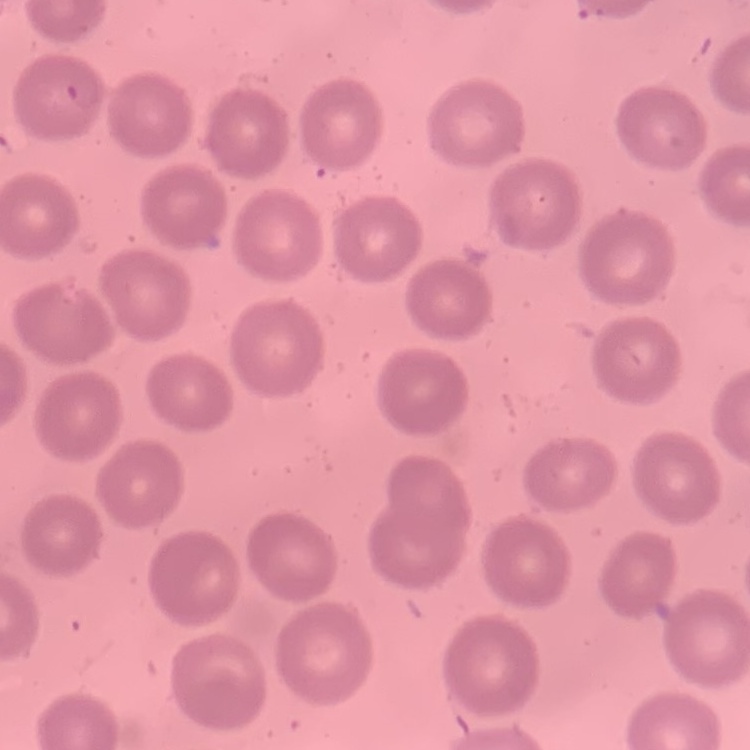

The erythrocytes exhibit no rouleaux formation. Thin peripheral smear. Field's or Giemsa stain. One tile cut from a larger photomicrograph.